Mark where platelets are.
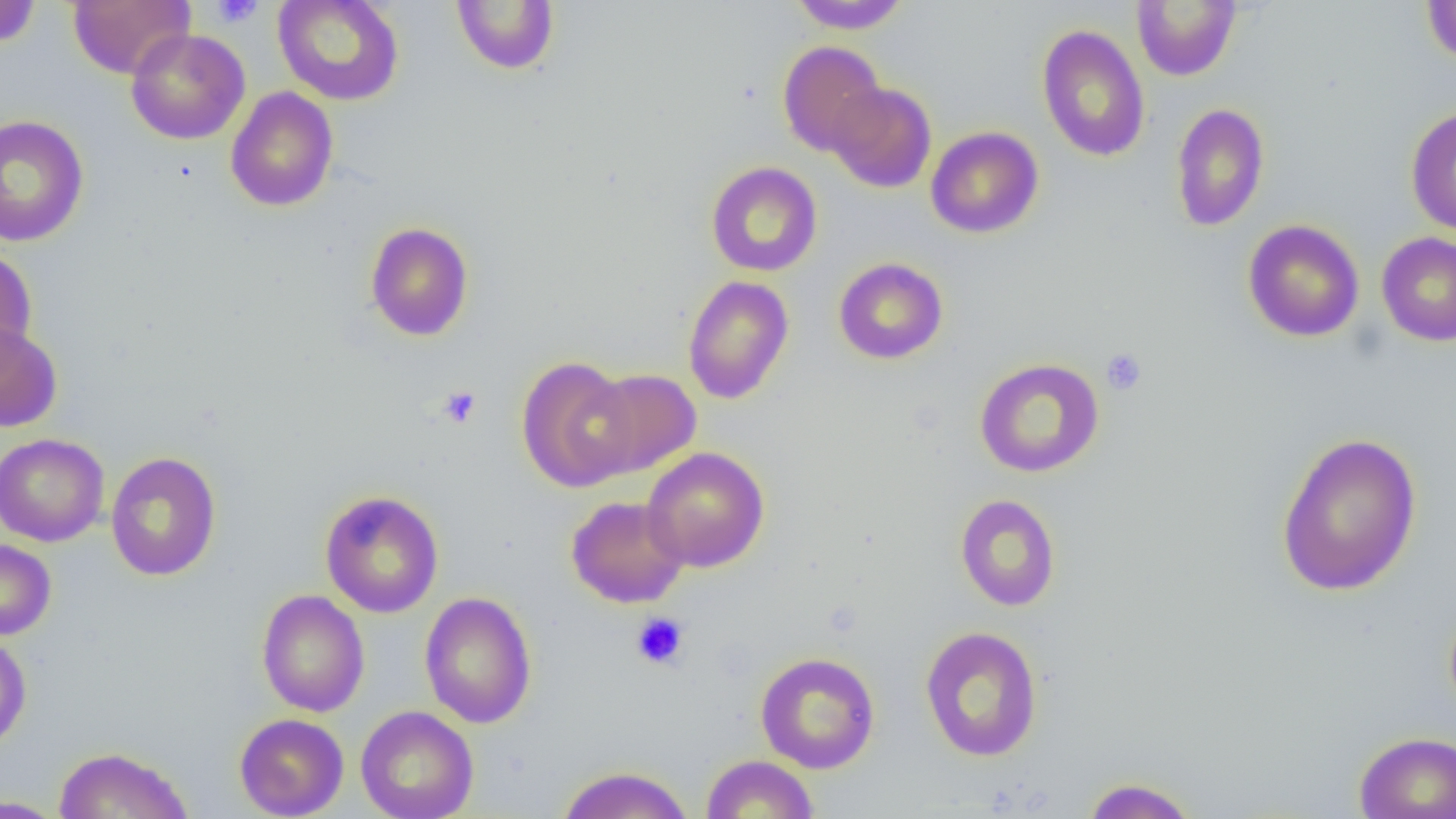
Approximate bounding boxes as named x1/y1/x2/y2 corners in pixels.
Platelets: (x1=211, y1=0, x2=264, y2=28), (x1=1101, y1=348, x2=1147, y2=395), (x1=437, y1=385, x2=481, y2=429), (x1=631, y1=613, x2=689, y2=669).

Uninfected red blood cell locations: (x1=0, y1=0, x2=42, y2=48), (x1=68, y1=0, x2=194, y2=79), (x1=272, y1=0, x2=405, y2=106), (x1=451, y1=1, x2=560, y2=74), (x1=787, y1=1, x2=912, y2=34), (x1=1132, y1=1, x2=1241, y2=81), (x1=1422, y1=1, x2=1456, y2=67), (x1=1036, y1=24, x2=1151, y2=162), (x1=125, y1=29, x2=250, y2=145), (x1=777, y1=41, x2=887, y2=157), (x1=826, y1=82, x2=937, y2=193), (x1=225, y1=86, x2=339, y2=212), (x1=1170, y1=102, x2=1270, y2=232), (x1=1405, y1=105, x2=1456, y2=236), (x1=0, y1=114, x2=90, y2=247), (x1=926, y1=126, x2=1044, y2=238), (x1=706, y1=161, x2=822, y2=277), (x1=1242, y1=219, x2=1365, y2=342), (x1=365, y1=221, x2=474, y2=341), (x1=1377, y1=232, x2=1456, y2=347), (x1=0, y1=246, x2=37, y2=366), (x1=833, y1=257, x2=948, y2=364), (x1=682, y1=275, x2=794, y2=405), (x1=0, y1=322, x2=62, y2=432), (x1=517, y1=356, x2=639, y2=492), (x1=974, y1=358, x2=1105, y2=478), (x1=582, y1=368, x2=702, y2=479), (x1=1274, y1=430, x2=1423, y2=598), (x1=0, y1=432, x2=109, y2=547), (x1=0, y1=444, x2=220, y2=557), (x1=642, y1=447, x2=770, y2=572), (x1=105, y1=451, x2=221, y2=581), (x1=319, y1=490, x2=444, y2=618), (x1=955, y1=494, x2=1061, y2=612), (x1=566, y1=495, x2=689, y2=608), (x1=0, y1=538, x2=56, y2=641), (x1=256, y1=589, x2=370, y2=717), (x1=419, y1=591, x2=537, y2=728), (x1=920, y1=625, x2=1043, y2=762), (x1=0, y1=632, x2=31, y2=753), (x1=755, y1=651, x2=880, y2=773), (x1=356, y1=705, x2=479, y2=819), (x1=234, y1=713, x2=349, y2=819), (x1=1354, y1=731, x2=1456, y2=819), (x1=54, y1=745, x2=194, y2=819), (x1=702, y1=754, x2=819, y2=818), (x1=556, y1=765, x2=694, y2=819), (x1=1081, y1=776, x2=1198, y2=819), (x1=0, y1=795, x2=67, y2=818). Slide-level diagnosis: negative for blood parasites. Optical microscopy. Thin blood film. Captured at 1000x magnification. Image is 1456×819 pixels. One field of a larger specimen.